Assess this cell for malaria.
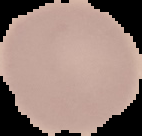

It is uninfected.

The area outside the segmented cell region is set to black. Image is 142×136 pixels. From a thin blood smear.